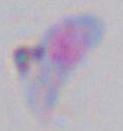
{
  "identification": "Toxoplasma gondii",
  "modality": "micrograph",
  "magnification": "1000x"
}